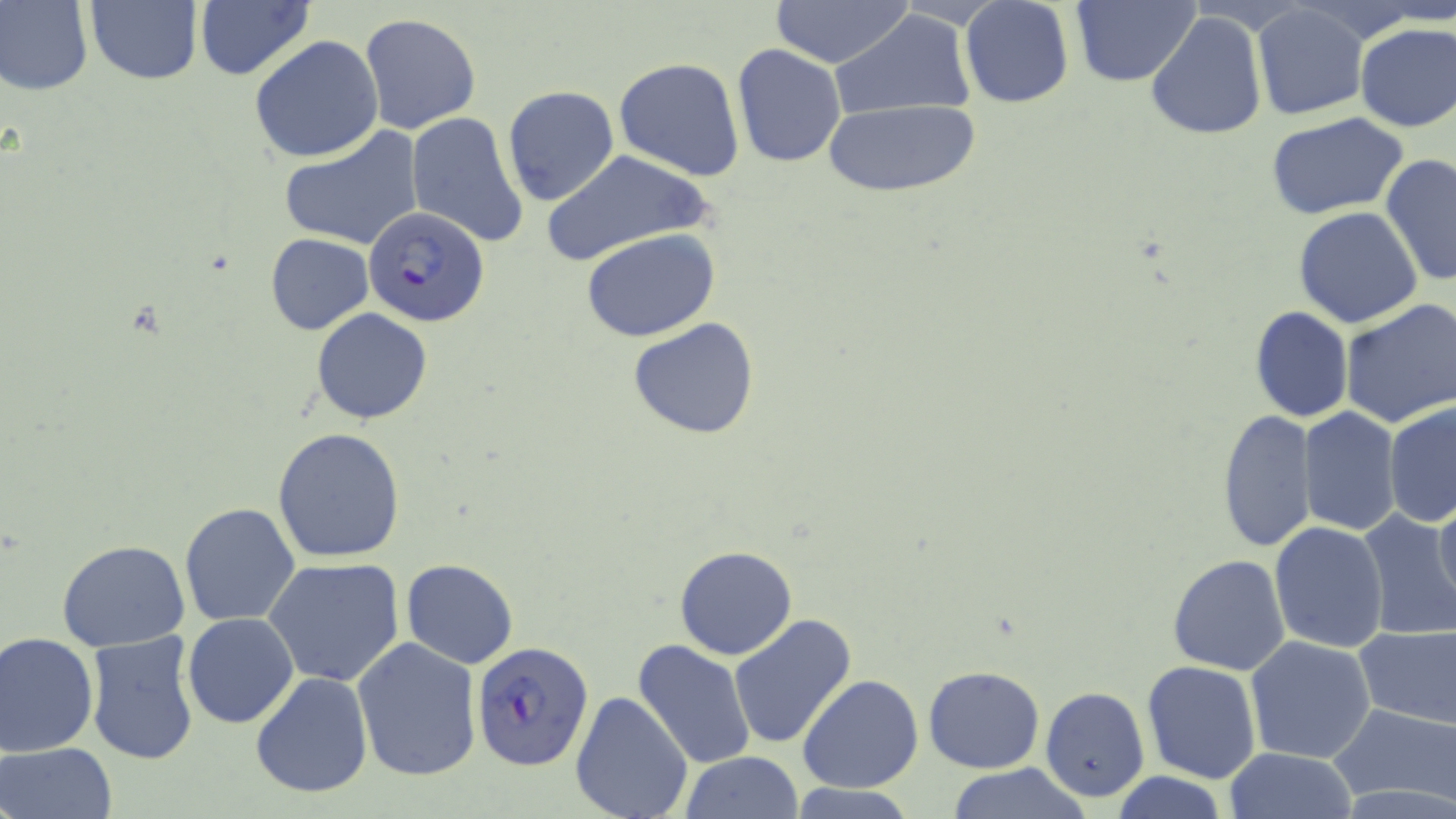
Approximate bounding boxes as named x1/y1/x2/y2 corners in pixels. Uninfected red blood cell locations: (x1=0, y1=0, x2=93, y2=96), (x1=84, y1=0, x2=202, y2=86), (x1=770, y1=0, x2=914, y2=67), (x1=1072, y1=0, x2=1201, y2=87), (x1=194, y1=1, x2=315, y2=82), (x1=959, y1=1, x2=1074, y2=109), (x1=1251, y1=3, x2=1369, y2=122), (x1=828, y1=11, x2=976, y2=121), (x1=1145, y1=11, x2=1269, y2=143), (x1=359, y1=13, x2=484, y2=136), (x1=1355, y1=22, x2=1456, y2=132), (x1=249, y1=34, x2=385, y2=163), (x1=730, y1=43, x2=847, y2=168), (x1=613, y1=56, x2=745, y2=182), (x1=501, y1=86, x2=620, y2=208), (x1=822, y1=99, x2=979, y2=199), (x1=1266, y1=111, x2=1410, y2=219), (x1=405, y1=112, x2=530, y2=251), (x1=280, y1=128, x2=424, y2=252), (x1=537, y1=147, x2=716, y2=267), (x1=1379, y1=154, x2=1455, y2=287), (x1=1293, y1=206, x2=1424, y2=329), (x1=582, y1=229, x2=721, y2=342), (x1=265, y1=233, x2=375, y2=334), (x1=1337, y1=299, x2=1455, y2=427), (x1=1248, y1=304, x2=1354, y2=424), (x1=311, y1=308, x2=432, y2=424), (x1=626, y1=316, x2=763, y2=440), (x1=1383, y1=401, x2=1456, y2=528), (x1=1216, y1=408, x2=1315, y2=555), (x1=1302, y1=408, x2=1402, y2=539), (x1=273, y1=428, x2=406, y2=562), (x1=1432, y1=494, x2=1456, y2=617), (x1=179, y1=502, x2=302, y2=627), (x1=1354, y1=509, x2=1456, y2=643), (x1=1269, y1=520, x2=1392, y2=654), (x1=57, y1=539, x2=190, y2=652), (x1=673, y1=545, x2=798, y2=660), (x1=1167, y1=554, x2=1291, y2=675), (x1=262, y1=556, x2=407, y2=686), (x1=400, y1=558, x2=518, y2=669), (x1=182, y1=613, x2=300, y2=729), (x1=730, y1=614, x2=858, y2=749), (x1=1354, y1=623, x2=1456, y2=731), (x1=85, y1=630, x2=200, y2=765), (x1=0, y1=631, x2=100, y2=756), (x1=1244, y1=635, x2=1376, y2=764), (x1=352, y1=636, x2=483, y2=780), (x1=632, y1=639, x2=758, y2=770), (x1=1141, y1=661, x2=1262, y2=783), (x1=922, y1=665, x2=1044, y2=774), (x1=250, y1=671, x2=374, y2=800), (x1=798, y1=675, x2=923, y2=793), (x1=1041, y1=686, x2=1150, y2=803), (x1=569, y1=689, x2=693, y2=819), (x1=1328, y1=700, x2=1456, y2=808), (x1=1, y1=741, x2=117, y2=819), (x1=1225, y1=748, x2=1356, y2=819), (x1=679, y1=752, x2=803, y2=819), (x1=943, y1=766, x2=1092, y2=819), (x1=1112, y1=772, x2=1230, y2=819), (x1=784, y1=784, x2=921, y2=818). Plasmodium falciparum-infected red blood cell locations: (x1=363, y1=206, x2=492, y2=330), (x1=471, y1=641, x2=595, y2=771). Slide-level diagnosis: Plasmodium falciparum. Captured at 1000x magnification. Thin blood film. Light microscopy. May-Grünwald-Giemsa-stained preparation. One field of a larger specimen. Image is 1456×819 pixels.